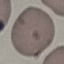

Summary:
  - Malaria status: uninfected
  - Preparation: thin blood smear
  - Stain: Giemsa
  - Image type: automatically extracted cell patch, resized to 64 × 64 pixels
  - Capture: smartphone camera at the microscope eyepiece